Describe the morphology of the red blood cells.
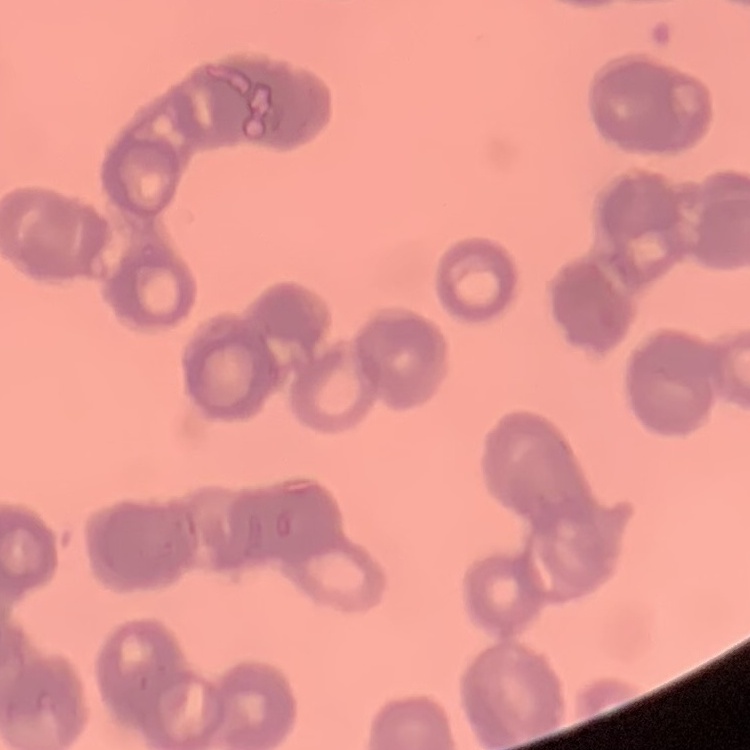
They show rouleaux formation.

preparation = thin blood smear
stain = Field's or Giemsa
image type = square crop of a larger photomicrograph